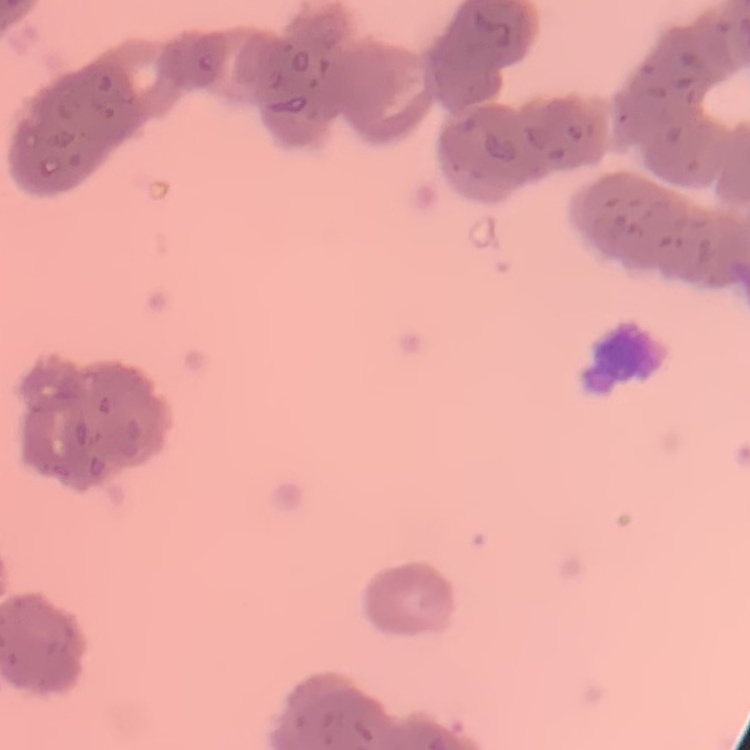

The erythrocytes show rouleaux formation. Stained with either Field's or Giemsa. Thin peripheral smear. Square crop of a larger photomicrograph.